Give the position of every Plasmodium parasite visible.
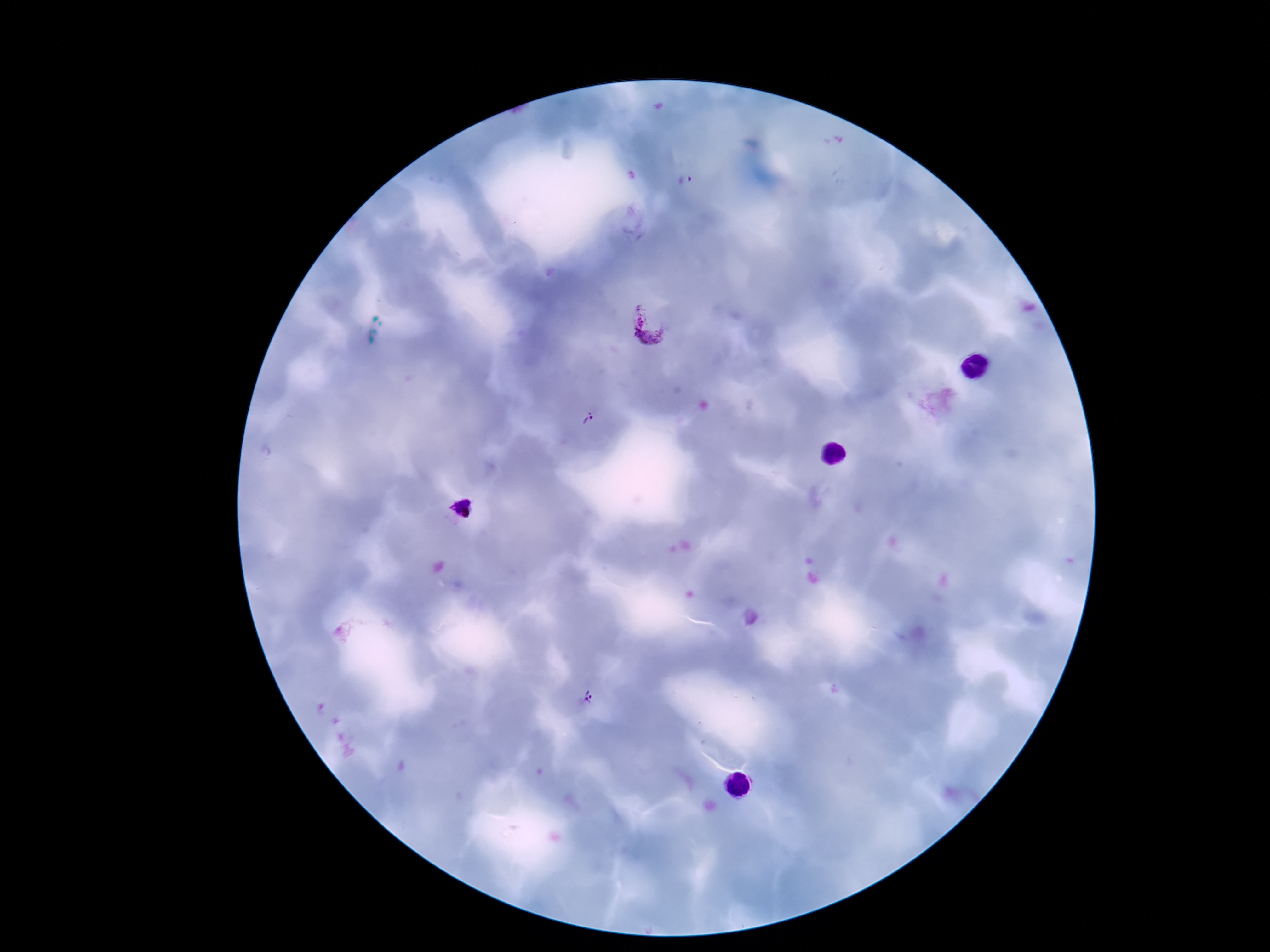

Approximate centers as [x, y] in pixels.
Plasmodium parasites: [687, 183], [646, 324], [588, 418], [461, 508], [588, 698].

Summary:
  - Patient malaria status: positive
  - Stain: Giemsa
  - Field of view: one from this slide
  - Capture: smartphone camera through the microscope eyepiece
  - Magnification: 100x
  - Image size: 1270×952 pixels
  - Preparation: thick peripheral-blood smear